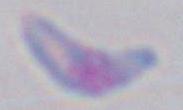
Summary:
  - Magnification: 1000x
  - Modality: photomicrograph
  - Identification: Toxoplasma gondii